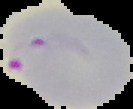
Result: malaria parasites identified. The area outside the segmented cell region is set to black. From a thin blood film. Image is 133×109 pixels.